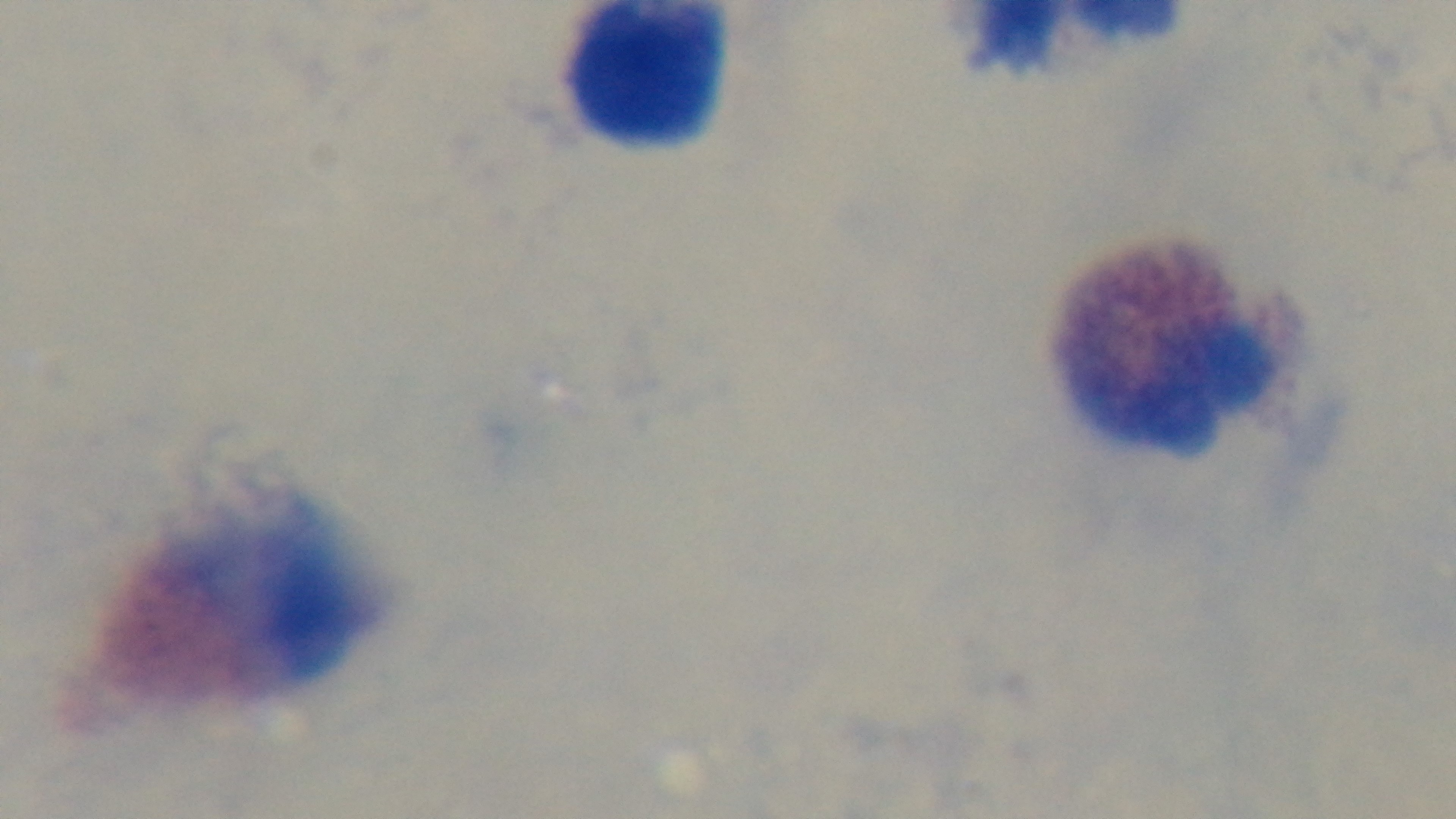
modality: light microscopy
objective: 100x oil immersion
capture: mounted 4K digital camera
field_of_view: single
malaria_status: negative
preparation: thick
stain: Giemsa